Name the blood parasite species.
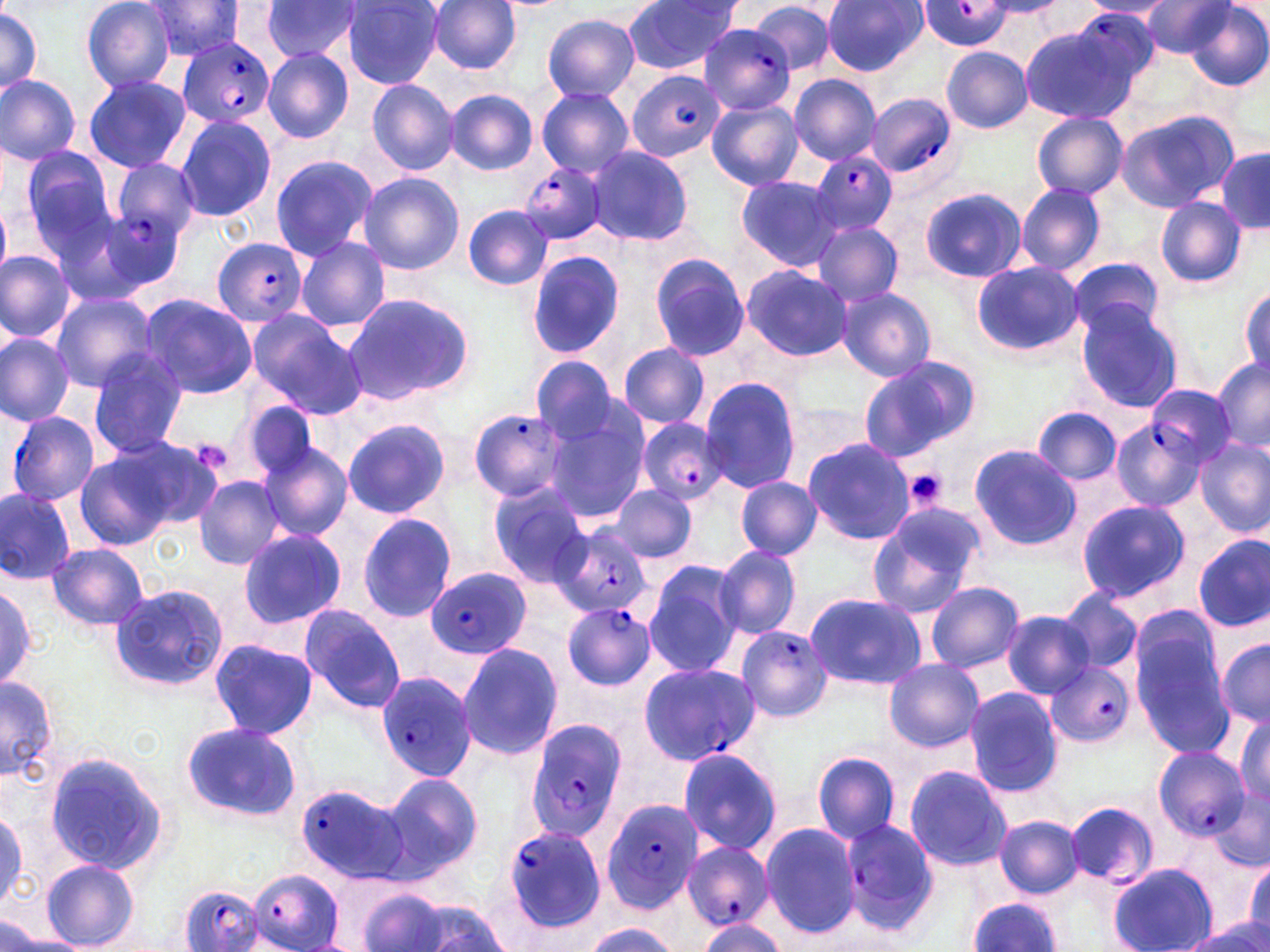

Plasmodium falciparum.

Approximate bounding boxes as (x1, y1, x2, y2) in pixels. Uninfected red blood cell locations: (80, 0, 178, 93), (142, 0, 249, 61), (427, 0, 522, 74), (822, 0, 928, 76), (623, 1, 742, 74), (1079, 1, 1172, 19), (1137, 1, 1235, 56), (260, 2, 361, 64), (342, 2, 443, 88), (749, 2, 835, 76), (1186, 4, 1270, 88), (0, 6, 42, 99), (542, 14, 640, 101), (1021, 31, 1132, 123), (941, 46, 1033, 133), (262, 48, 354, 143), (1, 73, 81, 166), (83, 74, 191, 173), (790, 74, 880, 164), (364, 78, 460, 175), (536, 87, 634, 176), (446, 90, 538, 175), (706, 99, 802, 190), (1115, 109, 1239, 211), (1031, 112, 1128, 199), (175, 114, 276, 221), (587, 146, 695, 247), (21, 148, 121, 255), (1215, 148, 1269, 232), (268, 154, 378, 261), (109, 157, 199, 237), (357, 172, 463, 274), (735, 175, 844, 272), (1016, 183, 1105, 275), (921, 187, 1027, 283), (1156, 197, 1246, 287), (0, 204, 11, 281), (464, 205, 553, 291), (814, 222, 903, 307), (294, 238, 389, 333), (0, 250, 75, 344), (526, 251, 627, 358), (649, 254, 754, 362), (1069, 257, 1167, 340), (971, 261, 1083, 356), (741, 265, 853, 361), (1240, 285, 1269, 381), (835, 286, 936, 382), (50, 292, 159, 392), (341, 292, 476, 407), (138, 293, 259, 399), (1076, 303, 1185, 414), (246, 310, 361, 416), (0, 333, 74, 425), (618, 344, 711, 429), (86, 348, 190, 456), (530, 356, 623, 443), (857, 358, 979, 462), (1212, 358, 1269, 452), (699, 377, 800, 493), (243, 401, 322, 481), (1033, 408, 1122, 487), (541, 411, 647, 522), (342, 419, 450, 519), (1111, 421, 1206, 513), (803, 438, 915, 545), (1195, 439, 1269, 535), (257, 443, 352, 542), (968, 443, 1081, 550), (71, 446, 189, 549), (194, 476, 285, 570), (735, 477, 822, 559), (488, 481, 593, 585), (608, 485, 697, 562), (0, 490, 75, 582), (1076, 499, 1190, 604), (864, 504, 983, 620), (357, 513, 456, 621), (236, 528, 348, 630), (1194, 534, 1270, 632), (47, 543, 150, 629), (713, 543, 802, 641), (643, 559, 743, 676), (925, 582, 1023, 673), (0, 585, 39, 692), (109, 585, 227, 691), (1055, 590, 1141, 676), (804, 592, 926, 690), (298, 603, 406, 712), (1003, 611, 1093, 699), (1128, 618, 1236, 757), (736, 627, 831, 722), (208, 638, 318, 739), (1215, 638, 1270, 729), (458, 641, 563, 760), (883, 659, 985, 752), (1, 674, 58, 784), (963, 687, 1064, 798), (1233, 714, 1269, 806), (180, 723, 303, 823), (677, 747, 785, 857), (813, 751, 902, 845), (44, 753, 168, 874), (903, 765, 1014, 872), (381, 772, 482, 877), (1207, 788, 1270, 874), (1067, 800, 1157, 887), (994, 816, 1083, 897), (760, 821, 862, 939), (40, 859, 139, 951), (1245, 859, 1270, 943), (1110, 864, 1214, 952), (354, 885, 455, 952), (968, 897, 1060, 952), (388, 898, 513, 950), (695, 917, 787, 951), (581, 922, 679, 951), (1183, 924, 1270, 952), (1, 928, 89, 951). Plasmodium falciparum-infected red blood cell locations: (920, 2, 1015, 50), (1076, 11, 1157, 81), (699, 24, 797, 117), (178, 37, 275, 131), (627, 70, 722, 162), (866, 93, 958, 181), (811, 150, 898, 235), (520, 161, 610, 245), (104, 208, 182, 287), (212, 238, 307, 327), (1144, 384, 1235, 466), (468, 408, 572, 503), (6, 410, 99, 506), (638, 416, 732, 507), (547, 526, 653, 619), (426, 568, 530, 658), (563, 602, 657, 691), (1046, 660, 1138, 749), (636, 662, 759, 767), (376, 672, 477, 783), (525, 715, 630, 843), (1152, 746, 1249, 839), (294, 783, 406, 883), (600, 797, 704, 913), (837, 819, 941, 936), (501, 824, 607, 936), (680, 840, 774, 931), (246, 872, 344, 950), (177, 884, 267, 952). Platelet locations: (190, 439, 234, 476), (902, 468, 948, 512). Thin blood film. May-Grünwald-Giemsa stain. Image is 1270×952 pixels. Captured at 1000x magnification. One field of a larger specimen. Light microscopy.